Identify the blood parasite species.
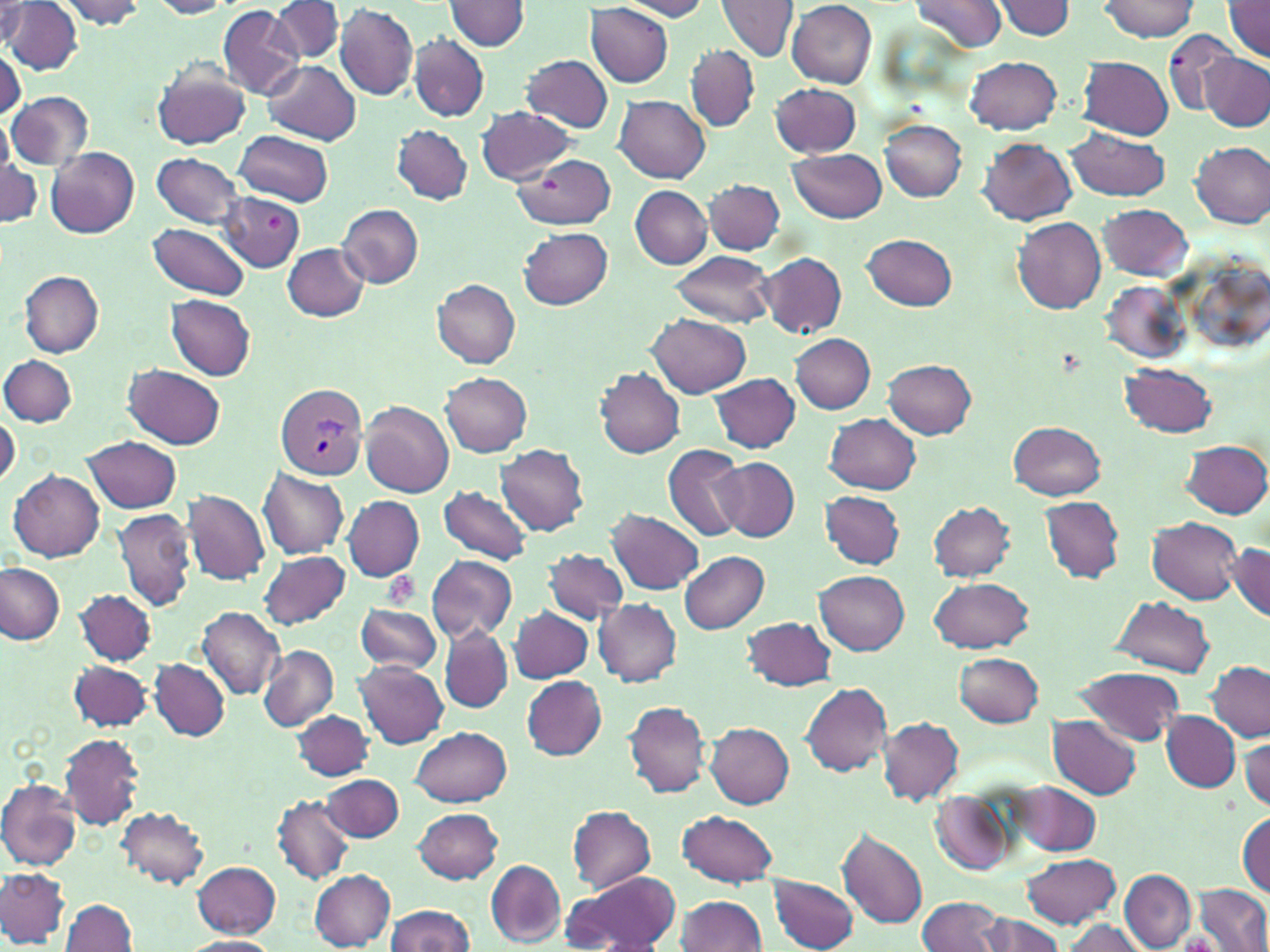
Plasmodium vivax.

Summary:
  - Coordinate format: approximate bounding boxes as (x1, y1, x2, y2) in pixels
  - Platelet locations: (267, 215, 282, 232), (382, 572, 420, 610)
  - Plasmodium vivax-infected red blood cell locations: (277, 384, 369, 480)
  - Uninfected red blood cell locations: (150, 0, 234, 18), (910, 0, 1009, 53), (1097, 0, 1199, 41), (4, 1, 83, 74), (54, 1, 149, 29), (270, 1, 344, 63), (446, 1, 531, 51), (616, 1, 713, 21), (716, 1, 797, 62), (786, 1, 876, 88), (995, 1, 1077, 40), (585, 2, 674, 87), (1, 3, 29, 49), (334, 3, 419, 102), (1222, 3, 1270, 61), (216, 4, 305, 102), (1164, 27, 1241, 116), (410, 35, 488, 120), (686, 45, 760, 131), (0, 47, 22, 124), (1199, 53, 1270, 131), (521, 55, 613, 133), (966, 57, 1063, 133), (1078, 57, 1173, 138), (263, 60, 360, 144), (153, 62, 252, 151), (771, 81, 860, 157), (7, 92, 93, 169), (614, 95, 710, 182), (476, 107, 576, 184), (882, 120, 967, 201), (393, 124, 472, 204), (1065, 128, 1170, 201), (235, 129, 333, 207), (977, 138, 1078, 226), (1191, 142, 1268, 227), (46, 147, 139, 238), (787, 148, 887, 223), (150, 152, 247, 229), (514, 153, 618, 230), (0, 158, 41, 227), (704, 179, 785, 253), (631, 186, 712, 268), (219, 192, 305, 273), (337, 203, 423, 286), (1098, 203, 1193, 281), (1012, 216, 1105, 312), (148, 222, 251, 300), (518, 227, 612, 308), (864, 233, 958, 309), (282, 242, 370, 323), (671, 252, 775, 326), (757, 252, 846, 337), (19, 271, 103, 357), (10, 274, 90, 427), (431, 277, 521, 367), (1100, 279, 1190, 365), (167, 295, 255, 380), (646, 312, 749, 397), (790, 333, 876, 414), (1, 355, 77, 427), (883, 360, 977, 437), (1120, 363, 1217, 436), (123, 364, 226, 448), (595, 367, 686, 458), (440, 374, 532, 456), (709, 374, 800, 453), (361, 400, 455, 498), (0, 413, 19, 488), (824, 413, 920, 494), (1009, 420, 1105, 500), (82, 436, 182, 514), (1182, 439, 1270, 518), (662, 442, 748, 543), (496, 444, 591, 535), (713, 457, 799, 543), (258, 468, 350, 559), (10, 469, 104, 562), (440, 486, 532, 567), (181, 490, 271, 586), (819, 490, 905, 570), (343, 495, 424, 581), (1040, 496, 1125, 582), (929, 501, 1016, 579), (113, 508, 197, 612), (608, 509, 704, 595), (1148, 517, 1242, 604), (1228, 540, 1270, 622), (543, 549, 628, 623), (259, 550, 350, 629), (679, 551, 770, 634), (426, 556, 517, 643), (1, 563, 65, 644), (817, 570, 908, 653), (929, 577, 1033, 652), (75, 590, 156, 665), (1110, 596, 1215, 675), (594, 599, 682, 686), (354, 603, 444, 673), (509, 605, 593, 683), (198, 607, 285, 699), (742, 615, 836, 690), (439, 627, 514, 712), (258, 645, 338, 730), (953, 652, 1044, 727), (68, 660, 153, 732), (150, 660, 230, 740), (356, 660, 449, 749), (1204, 662, 1269, 741), (1075, 667, 1184, 746), (521, 676, 606, 760), (801, 683, 892, 775), (625, 701, 709, 798), (292, 710, 373, 780), (1162, 711, 1239, 791), (1048, 715, 1142, 799), (876, 717, 964, 803), (706, 723, 793, 808), (412, 726, 511, 807), (59, 733, 145, 831), (1241, 734, 1270, 812), (320, 774, 403, 842), (0, 779, 82, 871), (1013, 781, 1102, 854), (931, 792, 1017, 877), (273, 795, 353, 884), (566, 805, 656, 893), (117, 806, 210, 889), (414, 807, 503, 883), (677, 809, 779, 888), (1237, 812, 1269, 897), (837, 828, 928, 929), (1021, 855, 1122, 928), (487, 860, 566, 945), (191, 861, 280, 938), (0, 866, 68, 948), (309, 870, 396, 950), (1119, 870, 1196, 951), (562, 872, 681, 952), (769, 875, 859, 950), (1197, 884, 1270, 951), (675, 895, 768, 952), (916, 895, 1004, 952), (60, 897, 136, 951), (383, 906, 478, 951), (977, 913, 1066, 952), (1060, 919, 1145, 952), (181, 936, 282, 952)
  - Modality: optical microscopy
  - Preparation: thin blood smear
  - Image size: 1270×952 pixels
  - Magnification: 1000x
  - Field of view: one of a larger specimen
  - Stain: May-Grünwald-Giemsa